Locate every uninfected red blood cell.
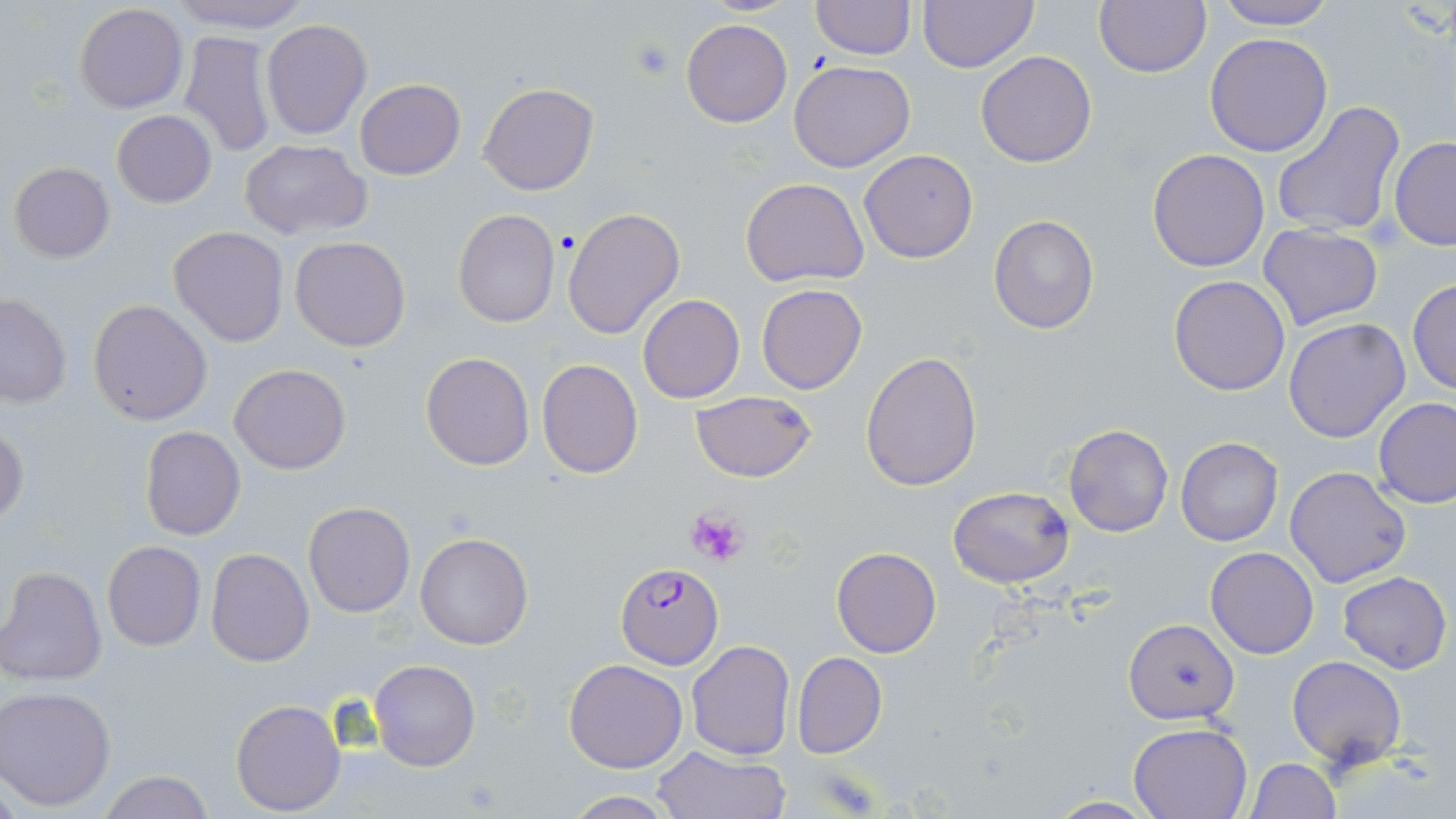

Approximate bounding boxes as (x1,y1)-(x2,y2) corner pairs in pixels.
Uninfected red blood cells: (164,0)-(314,32), (916,0)-(1039,72), (1093,0)-(1213,78), (1211,0)-(1339,30), (810,1)-(915,61), (74,3)-(188,114), (261,18)-(372,139), (681,18)-(793,127), (178,31)-(275,157), (1204,33)-(1333,156), (975,51)-(1097,168), (788,60)-(915,172), (355,78)-(465,181), (479,82)-(599,196), (1271,100)-(1405,240), (112,110)-(217,207), (1389,137)-(1456,250), (238,140)-(372,239), (858,149)-(979,263), (1147,149)-(1270,272), (8,162)-(114,263), (741,176)-(871,288), (562,206)-(685,340), (453,210)-(560,329), (987,213)-(1099,334), (1258,223)-(1383,331), (167,226)-(289,348), (289,236)-(413,352), (1169,274)-(1291,395), (1407,277)-(1455,396), (756,284)-(867,395), (0,292)-(72,409), (638,293)-(745,403), (88,299)-(213,426), (1283,318)-(1412,443), (420,351)-(535,469), (860,352)-(982,490), (537,358)-(642,477), (228,363)-(352,474), (689,391)-(818,483), (1374,397)-(1456,508), (0,422)-(29,528), (1063,422)-(1173,538), (139,426)-(246,542), (1175,436)-(1284,547), (1285,465)-(1413,588), (948,485)-(1075,587), (303,502)-(416,618), (414,532)-(534,649), (101,541)-(206,652), (831,547)-(942,657), (1206,547)-(1318,658), (206,548)-(313,665), (1,565)-(107,686), (1339,571)-(1451,673), (1124,619)-(1237,725), (685,640)-(795,759), (792,651)-(887,759), (1286,655)-(1407,771), (370,658)-(479,771), (563,658)-(687,772), (1,685)-(118,811), (229,698)-(347,816), (1129,721)-(1252,818), (651,746)-(790,818), (1246,757)-(1340,819), (97,771)-(218,819), (558,792)-(687,819), (1043,795)-(1163,818).

slide-level diagnosis = Plasmodium falciparum
platelet locations = approximate bounding boxes as (x1,y1)-(x2,y2) corner pairs in pixels: (629,37)-(676,83), (685,507)-(748,566)
modality = light microscopy
Plasmodium falciparum-infected red blood cell locations = approximate bounding boxes as (x1,y1)-(x2,y2) corner pairs in pixels: (615,562)-(724,668)
magnification = 1000x
stain = May-Grünwald-Giemsa
image size = 1456×819 pixels
field of view = one of a larger specimen
preparation = thin blood smear